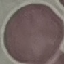 Malaria status: uninfected. Acquired by smartphone through the microscope eyepiece. Cell patch, automatically extracted from a larger field of view and resized to 64 × 64 pixels. Giemsa stain. Thin blood smear.